Locate and identify every blood parasite.
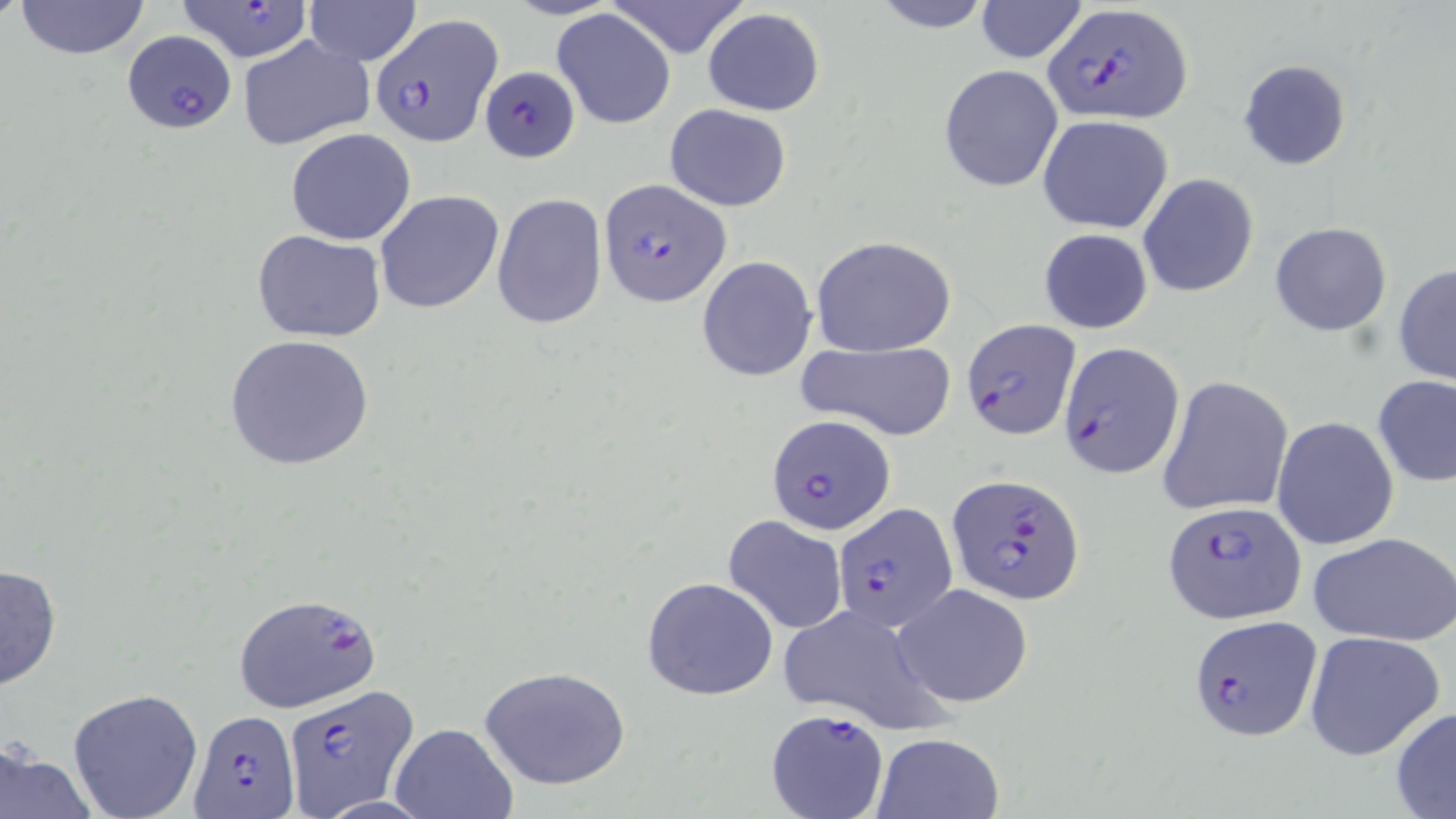

Approximate bounding boxes as (x1,y1)-(x2,y2) corner pairs in pixels.
Plasmodium falciparum-infected red blood cells (subset): (173,1)-(315,59), (1041,4)-(1192,126), (373,12)-(500,144), (122,30)-(240,133), (481,63)-(580,161), (598,178)-(732,306), (1059,343)-(1184,479), (767,414)-(896,537), (947,473)-(1084,604), (1162,501)-(1305,623), (833,502)-(953,635), (235,594)-(381,714), (1187,614)-(1322,740), (284,688)-(418,812), (765,707)-(889,818), (190,710)-(301,815).
No Plasmodium ovale, Plasmodium malariae, Plasmodium vivax, Babesia divergens, or Trypanosoma brucei observed.

Summary:
  - Uninfected red blood cell locations (subset): (12,0)-(151,60), (303,0)-(421,65), (608,0)-(751,59), (866,0)-(997,33), (975,0)-(1089,63), (552,8)-(676,128), (703,8)-(825,116), (237,35)-(375,151), (1237,59)-(1352,171), (938,64)-(1064,192), (665,103)-(792,212), (1037,115)-(1173,234), (285,127)-(417,245), (1138,173)-(1259,298), (376,190)-(505,315), (491,192)-(607,330), (1269,221)-(1392,337), (1038,228)-(1153,335), (252,230)-(387,343), (810,235)-(956,356), (697,255)-(818,380), (1393,263)-(1456,386), (225,334)-(376,473), (794,339)-(957,441), (1372,374)-(1456,489), (1159,375)-(1294,517), (1272,416)-(1399,551), (723,515)-(849,635), (1308,531)-(1456,645), (0,561)-(64,691), (641,575)-(778,701), (894,583)-(1034,708), (776,605)-(945,736), (1303,630)-(1445,761), (478,664)-(633,791), (67,687)-(203,818), (1390,706)-(1456,817), (388,723)-(518,819), (871,733)-(1003,818), (0,741)-(95,819)
  - Slide-level diagnosis: Plasmodium falciparum
  - Field of view: single
  - Preparation: thin blood smear
  - Image size: 1456×819 pixels
  - Modality: light microscopy
  - Stain: May-Grünwald-Giemsa
  - Magnification: 1000x